Give the position of every Plasmodium parasite.
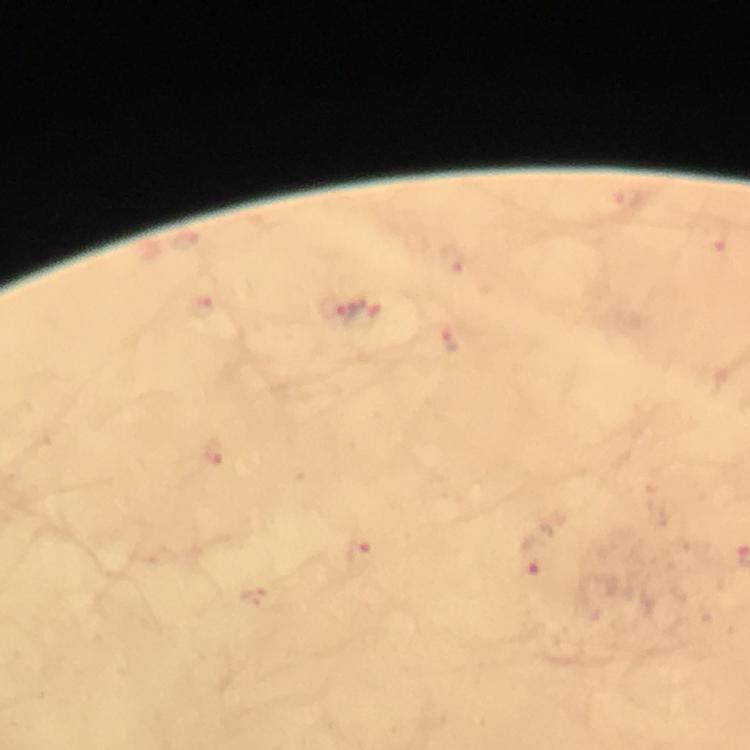
Approximate centers as {x, y} in pixels.
Plasmodium parasites: {629, 199}, {186, 240}, {718, 240}, {452, 260}, {331, 307}, {210, 308}, {364, 315}, {450, 343}, {214, 451}, {361, 553}, {531, 557}.

magnification: 100x
image_size: 750×750 pixels
preparation: thick smear
cropped_from: one field of view
capture: smartphone camera through the microscope
immersion_oil: used
stain: Giemsa
context: from a diagnostic examination for malaria